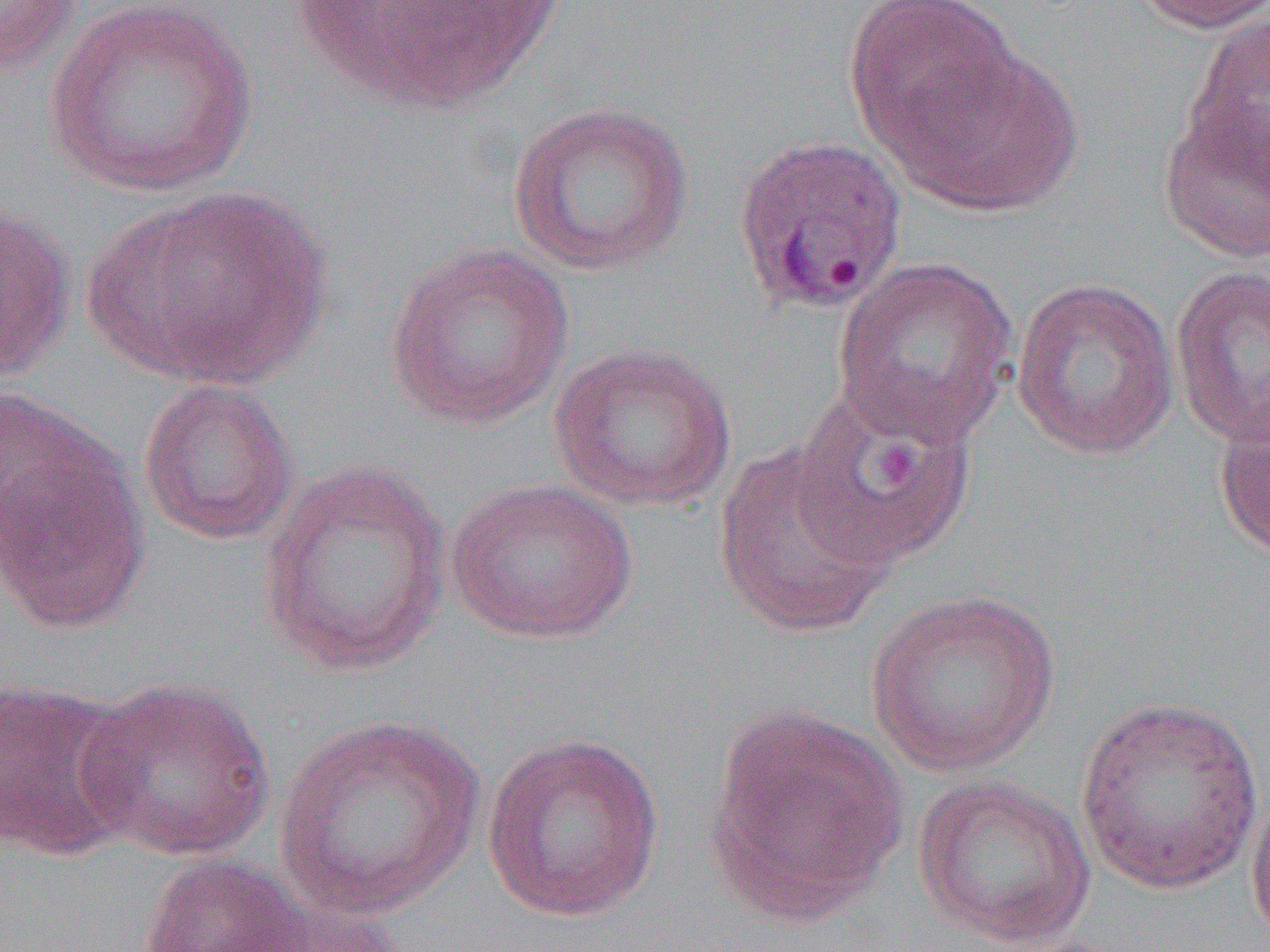

Approximate bounding boxes as [x1, y1, x2, y2] in pixels. Platelet locations: [868, 434, 924, 490]. Plasmodium ovale-infected red blood cell locations: [732, 134, 909, 316]. Uninfected red blood cell locations (subset): [0, 0, 81, 79], [43, 0, 260, 198], [845, 0, 1023, 159], [1127, 0, 1270, 35], [1181, 12, 1269, 187], [890, 44, 1083, 217], [506, 100, 695, 277], [1158, 102, 1270, 264], [85, 185, 335, 390], [0, 202, 77, 383], [384, 241, 575, 430], [830, 255, 1019, 445], [1169, 264, 1270, 448], [1010, 277, 1181, 461], [548, 341, 737, 513], [137, 378, 299, 545], [791, 385, 978, 568], [1213, 399, 1270, 567], [1, 420, 149, 638], [712, 443, 899, 638], [257, 460, 454, 677], [446, 476, 639, 644], [865, 589, 1060, 777], [77, 676, 276, 861], [0, 678, 141, 860], [1074, 696, 1265, 896], [703, 703, 910, 926], [271, 714, 487, 920], [480, 731, 666, 924], [912, 773, 1097, 950], [1245, 786, 1270, 948], [136, 853, 309, 952], [230, 896, 411, 952]. Slide-level diagnosis: Plasmodium ovale. Thin blood film. Light microscopy. 1000x magnification. Single field of view. Image is 1270×952 pixels.